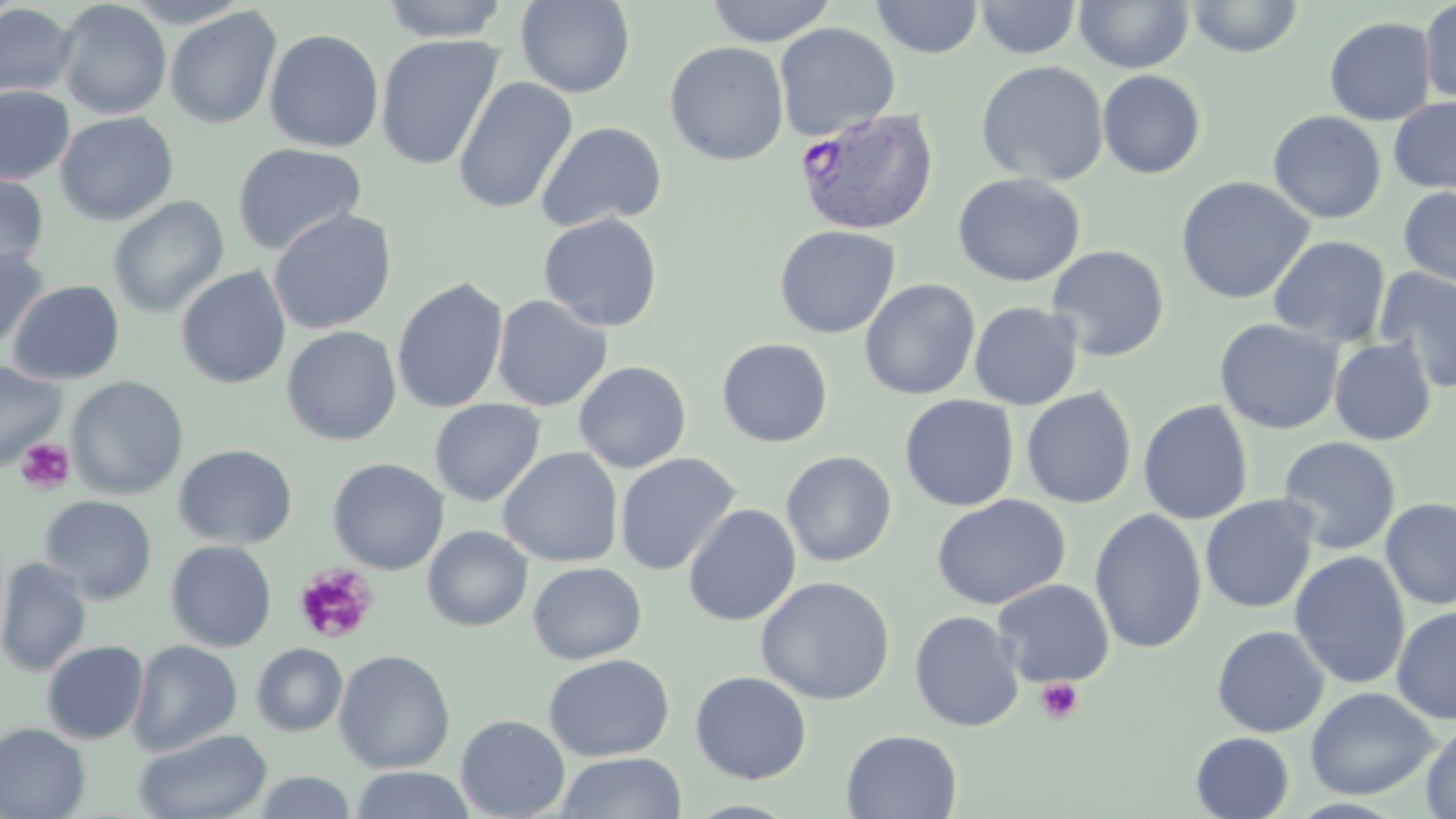

{
  "slide_level_diagnosis": "Plasmodium vivax",
  "field_of_view": "single",
  "stain": "May-Grünwald-Giemsa",
  "plasmodium_vivax_infected_red_blood_cell_locations": "approximate bounding boxes as (x1,y1)-(x2,y2) corner pairs in pixels: (795,107)-(940,236)",
  "modality": "optical microscopy",
  "platelet_locations": "approximate bounding boxes as (x1,y1)-(x2,y2) corner pairs in pixels: (15,437)-(76,495), (293,564)-(379,645), (1035,677)-(1084,726)",
  "uninfected_red_blood_cell_locations": "approximate bounding boxes as (x1,y1)-(x2,y2) corner pairs in pixels: (55,0)-(172,119), (380,0)-(510,43), (706,0)-(837,47), (872,0)-(984,59), (975,0)-(1082,59), (1074,0)-(1194,74), (1187,0)-(1304,58), (515,1)-(636,98), (1419,2)-(1456,106), (0,3)-(78,100), (165,7)-(282,129), (1324,17)-(1436,125), (774,23)-(901,141), (264,28)-(384,153), (375,34)-(504,171), (665,41)-(789,166), (975,61)-(1109,187), (1097,69)-(1207,179), (453,76)-(578,214), (0,85)-(75,185), (1388,96)-(1456,193), (1267,110)-(1386,224), (55,111)-(178,226), (536,122)-(666,232), (232,142)-(366,256), (0,171)-(50,276), (952,172)-(1086,287), (1175,176)-(1314,305), (1398,186)-(1456,289), (107,196)-(229,318), (267,208)-(397,335), (538,213)-(663,332), (774,225)-(901,338), (1268,235)-(1391,348), (0,245)-(49,354), (1046,245)-(1170,362), (176,266)-(291,389), (1373,268)-(1456,393), (391,277)-(509,414), (859,278)-(980,400), (7,279)-(125,385), (491,295)-(612,411), (968,301)-(1084,411), (1214,318)-(1343,434), (281,326)-(401,446), (716,337)-(833,448), (1328,338)-(1437,446), (573,360)-(692,473), (0,361)-(66,470), (66,376)-(189,500), (1020,387)-(1137,509), (899,395)-(1019,511), (429,399)-(545,506), (1137,399)-(1254,525), (1277,436)-(1402,555), (173,443)-(297,549), (499,446)-(623,568), (781,450)-(897,567), (614,453)-(740,575), (327,458)-(449,575), (931,494)-(1071,610), (39,495)-(157,605), (1200,495)-(1318,614), (1380,497)-(1456,610), (683,504)-(801,626), (1089,508)-(1207,653), (422,525)-(533,632), (165,540)-(277,652), (1288,551)-(1412,689), (0,557)-(92,677), (527,562)-(647,665), (756,576)-(895,706), (992,579)-(1115,687), (1391,605)-(1456,724), (909,610)-(1025,732), (1211,625)-(1329,737), (127,639)-(243,756), (42,640)-(149,745), (251,643)-(348,736), (334,649)-(456,773), (543,653)-(674,761), (690,671)-(812,784), (1305,687)-(1439,800), (456,714)-(570,819), (1421,722)-(1456,818), (0,723)-(90,819), (134,728)-(273,819), (841,729)-(962,819), (1190,732)-(1295,819), (555,751)-(687,818), (349,766)-(476,819), (253,770)-(357,818)",
  "preparation": "thin blood film",
  "image_size": "1456×819 pixels",
  "magnification": "1000x"
}